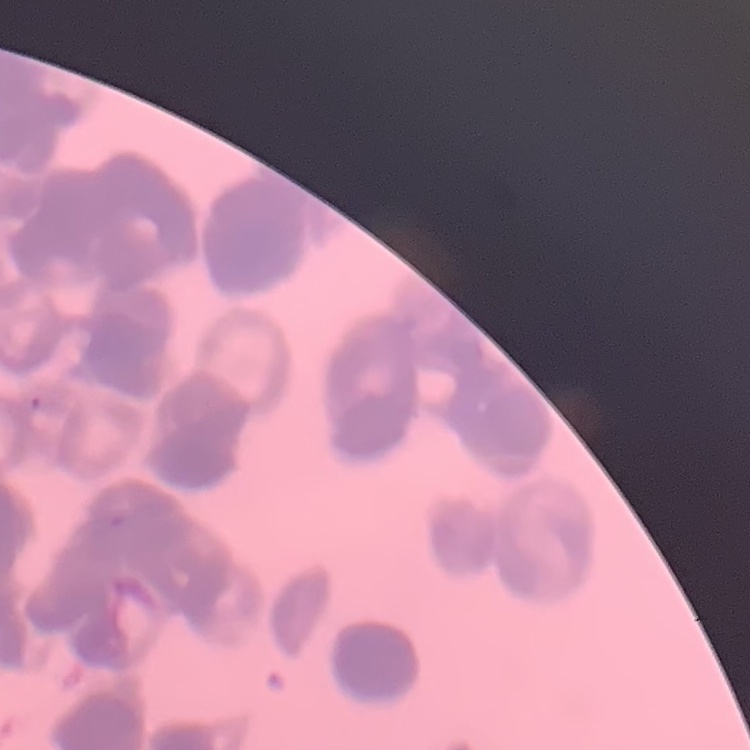
The erythrocytes exhibit rouleaux formation. Square crop of a larger photomicrograph. Field's or Giemsa stain. Thin blood film.